Classify this cell by malaria status.
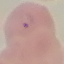

It is parasitized.

Summary:
  - Image type: cell patch, automatically extracted from a larger field of view and resized to 64 × 64 pixels
  - Stain: Giemsa
  - Preparation: thin smear
  - Capture: smartphone through the microscope eyepiece